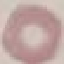
Summary:
  - Malaria status: uninfected
  - Stain: Giemsa
  - Image type: cell patch, automatically extracted from a larger field of view and resized to 64 × 64 pixels
  - Capture: smartphone camera at the microscope eyepiece
  - Preparation: thin blood smear